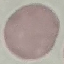
Summary:
  - Result: negative for malaria parasites
  - Preparation: thin blood film
  - Capture: smartphone through the microscope eyepiece
  - Image type: automatically extracted cell patch, resized to 64 × 64 pixels
  - Stain: Giemsa